Classify this cell by malaria status.
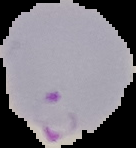

Parasitized.

Segmented cell region on a black background. Image is 136×148 pixels. From a thin blood film.